State which parasite is depicted.
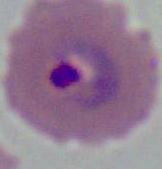
This is Plasmodium.

400x or 1000x magnification. Micrograph.